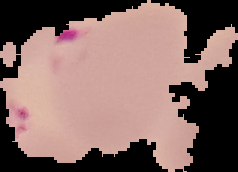 Image is 238×172 pixels. The area outside the segmented cell region is set to black. From a thin blood smear. Malaria status: parasitized.